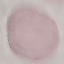
result = negative for malaria parasites
stain = Giemsa
capture = smartphone through the microscope eyepiece
preparation = thin smear
image type = cell patch, automatically extracted from a larger field of view and resized to 64 × 64 pixels